Locate and identify every blood parasite.
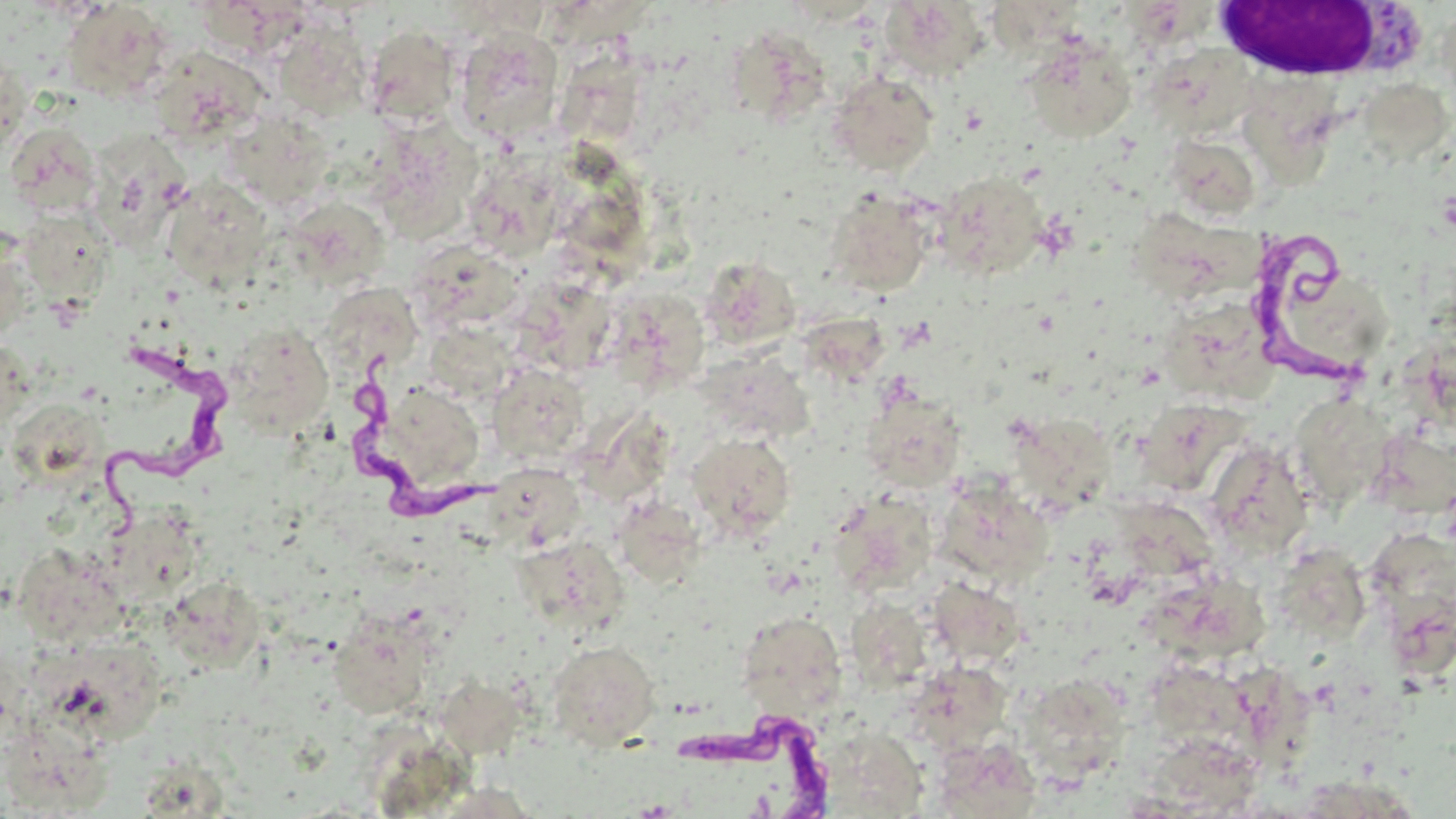
Approximate bounding boxes as [x1, y1, x2, y2] in pixels.
Trypanosoma brucei: [1247, 234, 1374, 388], [95, 336, 241, 529], [354, 342, 500, 522], [670, 699, 837, 818].
No Plasmodium falciparum, Plasmodium ovale, Plasmodium malariae, Plasmodium vivax, or Babesia divergens observed.

White blood cell locations: [1203, 1, 1412, 82]. Uninfected red blood cell locations: [879, 0, 991, 81], [61, 2, 174, 101], [1117, 5, 1211, 56], [989, 6, 1089, 69], [273, 17, 374, 122], [363, 24, 460, 126], [453, 26, 564, 142], [1023, 34, 1137, 143], [732, 35, 831, 127], [1145, 44, 1258, 139], [148, 48, 269, 146], [1, 51, 28, 159], [571, 59, 647, 141], [827, 71, 940, 175], [1357, 78, 1455, 164], [1255, 85, 1347, 190], [223, 112, 334, 208], [4, 121, 103, 217], [371, 122, 483, 235], [92, 131, 194, 250], [1169, 141, 1249, 222], [463, 157, 569, 261], [934, 170, 1048, 280], [161, 177, 273, 288], [825, 188, 936, 296], [575, 204, 660, 285], [299, 206, 389, 285], [16, 210, 114, 302], [1144, 215, 1260, 294], [0, 226, 37, 339], [428, 249, 525, 324], [702, 256, 804, 350], [1295, 278, 1394, 368], [318, 289, 426, 365], [525, 289, 614, 383], [609, 293, 701, 379], [1170, 312, 1275, 412], [796, 314, 894, 385], [225, 321, 334, 440], [1404, 334, 1456, 431], [0, 335, 30, 436], [700, 352, 819, 450], [487, 363, 591, 464], [393, 384, 491, 482], [861, 389, 967, 492], [1287, 393, 1396, 512], [13, 399, 117, 490], [1149, 403, 1244, 495], [578, 413, 685, 499], [1016, 428, 1119, 511], [686, 432, 796, 541], [1380, 435, 1456, 519], [1212, 440, 1306, 557], [504, 474, 586, 549], [949, 491, 1051, 585], [833, 495, 929, 591], [629, 505, 713, 591], [1115, 506, 1227, 589], [103, 509, 209, 603], [1369, 525, 1455, 603], [20, 542, 131, 648], [520, 543, 630, 641], [1282, 557, 1367, 647], [1142, 577, 1276, 672], [927, 578, 1026, 667], [164, 581, 261, 670], [1377, 588, 1452, 668], [851, 602, 929, 696], [736, 611, 847, 719], [335, 616, 432, 715], [24, 636, 169, 751], [547, 640, 661, 750], [1138, 655, 1262, 746], [1225, 667, 1308, 780], [924, 669, 1008, 750], [1023, 671, 1123, 782], [442, 682, 519, 765], [816, 725, 929, 817], [7, 731, 115, 814], [930, 736, 1044, 817], [1154, 737, 1255, 816], [145, 763, 231, 818], [1303, 773, 1428, 819]. Slide-level diagnosis: Trypanosoma brucei. Light microscopy. One field of a larger specimen. Image is 1456×819 pixels. May-Grünwald-Giemsa stain. Thin blood film. 1000x magnification.